Name the parasite shown.
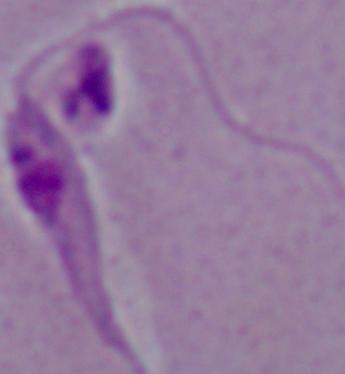

This is Leishmania.

Photomicrograph. 1000x magnification.